Report the malaria status of this cell.
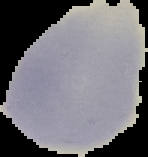

It is uninfected.

Summary:
  - Image size: 148×157 pixels
  - Preparation: thin blood film
  - Image type: segmented cell region on a black background